Locate every Plasmodium parasite.
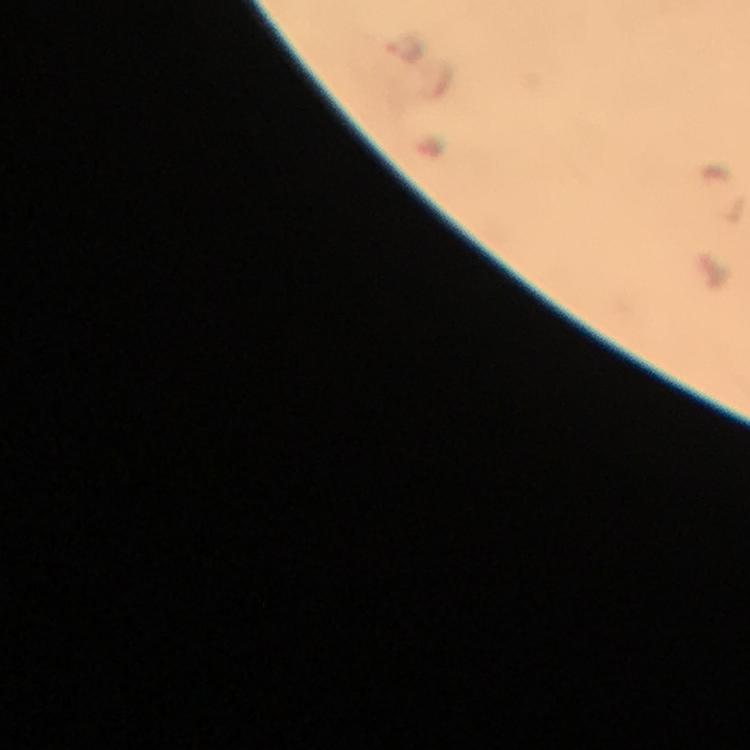
Approximate centers as [x, y] in pixels.
Plasmodium parasites: [404, 48].

immersion oil = applied
context = from a malaria diagnostic workup
image size = 750×750 pixels
preparation = thick smear
magnification = 100x
cropped from = one field of view
capture = smartphone mounted on the microscope
stain = Giemsa